Comment on the morphology of the erythrocytes.
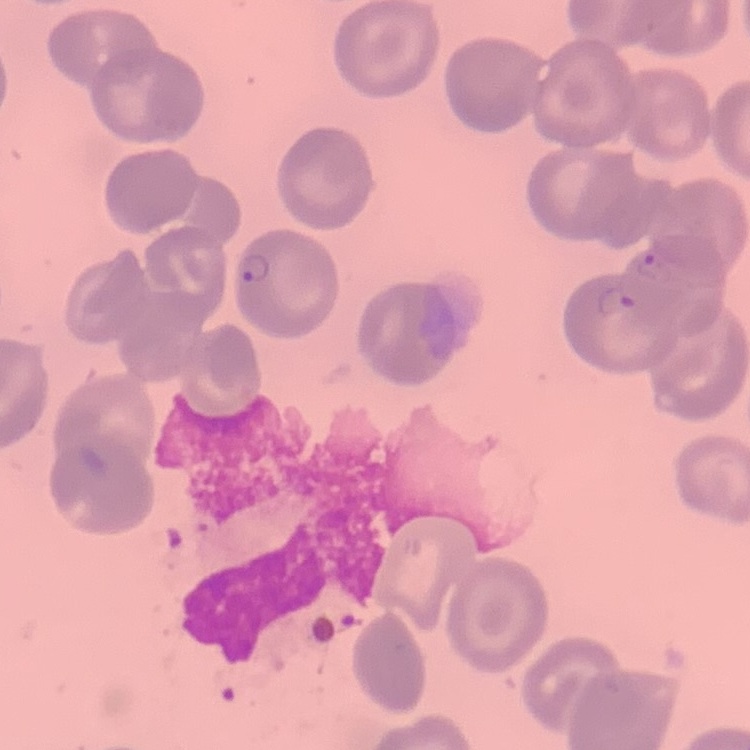
No rouleaux formation.

{
  "preparation": "thin peripheral smear",
  "image_type": "square crop of a larger photomicrograph",
  "stain": "Field's or Giemsa"
}